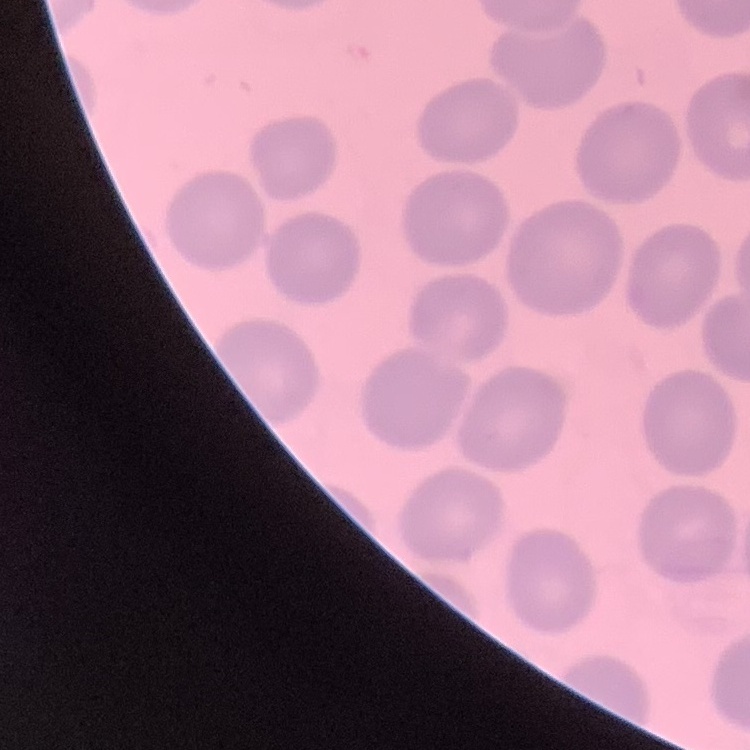

Summary:
  - Erythrocyte morphology: no rouleaux formation
  - Image type: one tile cut from a larger photomicrograph
  - Stain: Field's or Giemsa
  - Preparation: thin blood smear